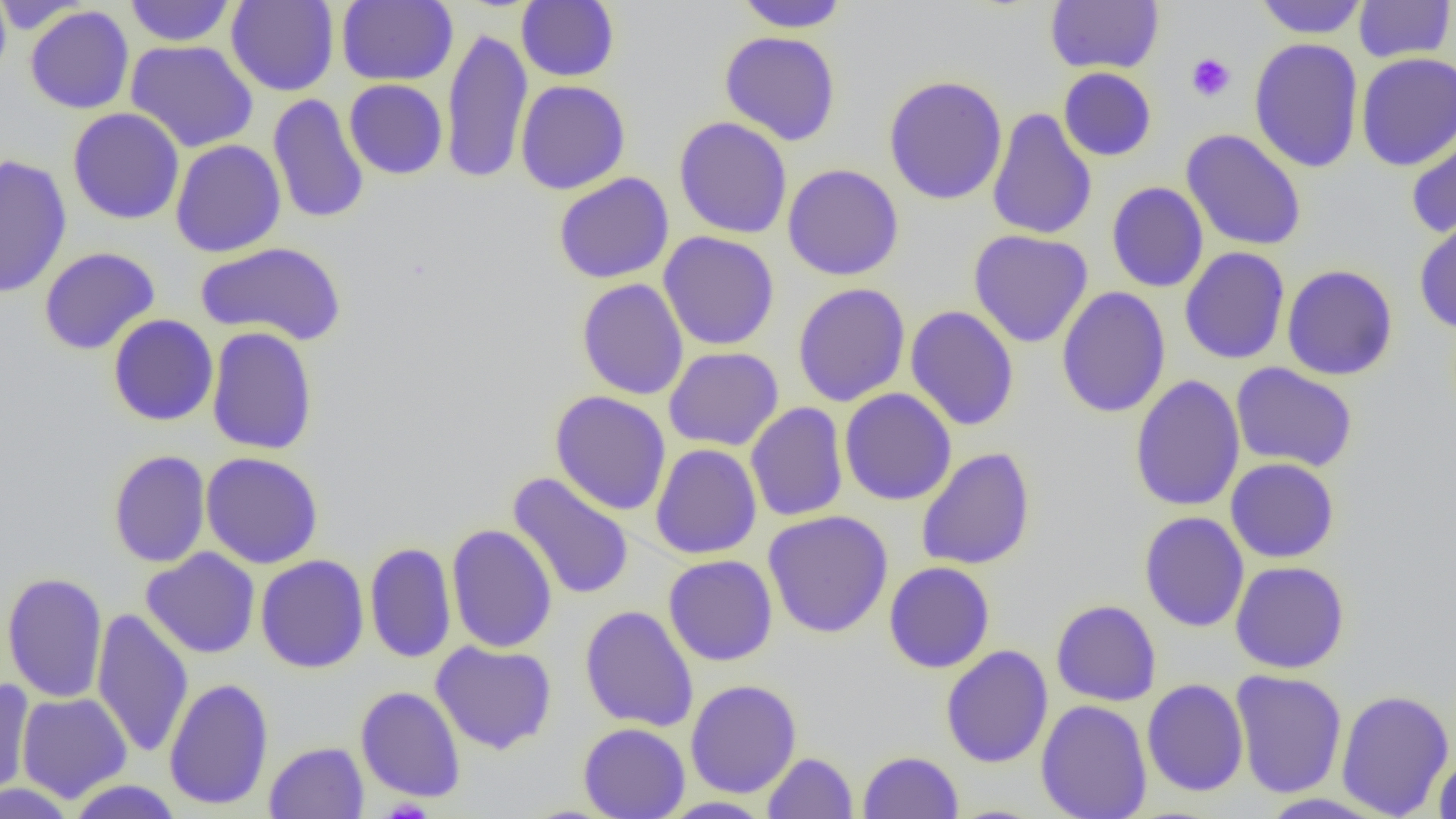 Approximate bounding boxes as named x1/y1/x2/y2 corners in pixels. Platelet locations: (x1=1186, y1=53, x2=1236, y2=102). Uninfected red blood cell locations: (x1=0, y1=0, x2=11, y2=86), (x1=124, y1=0, x2=236, y2=47), (x1=226, y1=0, x2=339, y2=96), (x1=336, y1=0, x2=458, y2=86), (x1=733, y1=0, x2=850, y2=33), (x1=1254, y1=0, x2=1368, y2=38), (x1=1353, y1=0, x2=1455, y2=63), (x1=0, y1=1, x2=91, y2=36), (x1=516, y1=1, x2=620, y2=82), (x1=1046, y1=1, x2=1164, y2=74), (x1=25, y1=6, x2=134, y2=113), (x1=440, y1=28, x2=533, y2=185), (x1=719, y1=30, x2=841, y2=146), (x1=1249, y1=37, x2=1364, y2=173), (x1=126, y1=39, x2=258, y2=153), (x1=1356, y1=52, x2=1456, y2=171), (x1=1058, y1=67, x2=1157, y2=162), (x1=883, y1=75, x2=1008, y2=205), (x1=344, y1=79, x2=448, y2=179), (x1=515, y1=80, x2=631, y2=195), (x1=268, y1=93, x2=369, y2=224), (x1=68, y1=107, x2=185, y2=224), (x1=987, y1=107, x2=1097, y2=241), (x1=674, y1=116, x2=792, y2=239), (x1=1405, y1=118, x2=1456, y2=241), (x1=1181, y1=129, x2=1307, y2=251), (x1=170, y1=139, x2=286, y2=257), (x1=0, y1=154, x2=72, y2=298), (x1=783, y1=163, x2=904, y2=281), (x1=553, y1=172, x2=674, y2=284), (x1=1106, y1=182, x2=1209, y2=292), (x1=1414, y1=216, x2=1456, y2=334), (x1=968, y1=229, x2=1094, y2=348), (x1=659, y1=231, x2=780, y2=350), (x1=195, y1=241, x2=347, y2=346), (x1=39, y1=247, x2=160, y2=355), (x1=1179, y1=247, x2=1290, y2=365), (x1=1281, y1=264, x2=1399, y2=381), (x1=576, y1=278, x2=689, y2=400), (x1=793, y1=283, x2=910, y2=407), (x1=1056, y1=286, x2=1171, y2=418), (x1=905, y1=305, x2=1019, y2=431), (x1=107, y1=314, x2=218, y2=426), (x1=206, y1=326, x2=319, y2=455), (x1=663, y1=346, x2=784, y2=451), (x1=1230, y1=362, x2=1358, y2=472), (x1=1129, y1=375, x2=1245, y2=512), (x1=839, y1=388, x2=957, y2=505), (x1=549, y1=391, x2=671, y2=515), (x1=746, y1=402, x2=849, y2=522), (x1=650, y1=443, x2=762, y2=559), (x1=916, y1=447, x2=1036, y2=570), (x1=108, y1=449, x2=210, y2=568), (x1=201, y1=451, x2=324, y2=569), (x1=1225, y1=458, x2=1339, y2=563), (x1=508, y1=473, x2=634, y2=601), (x1=763, y1=510, x2=893, y2=638), (x1=1138, y1=512, x2=1249, y2=632), (x1=445, y1=523, x2=558, y2=653), (x1=364, y1=541, x2=457, y2=664), (x1=141, y1=547, x2=260, y2=659), (x1=255, y1=554, x2=370, y2=673), (x1=663, y1=554, x2=778, y2=666), (x1=1230, y1=560, x2=1350, y2=674), (x1=884, y1=561, x2=996, y2=673), (x1=1, y1=572, x2=108, y2=703), (x1=1051, y1=599, x2=1161, y2=706), (x1=579, y1=605, x2=699, y2=732), (x1=92, y1=607, x2=193, y2=759), (x1=430, y1=640, x2=557, y2=754), (x1=940, y1=645, x2=1053, y2=768), (x1=1230, y1=669, x2=1348, y2=799), (x1=163, y1=678, x2=274, y2=810), (x1=1141, y1=678, x2=1249, y2=796), (x1=0, y1=679, x2=35, y2=802), (x1=685, y1=679, x2=802, y2=798), (x1=355, y1=686, x2=467, y2=803), (x1=1335, y1=688, x2=1454, y2=818), (x1=16, y1=692, x2=132, y2=802), (x1=1036, y1=699, x2=1153, y2=819), (x1=578, y1=723, x2=690, y2=819), (x1=264, y1=741, x2=369, y2=818), (x1=1434, y1=749, x2=1456, y2=818), (x1=858, y1=750, x2=964, y2=818), (x1=763, y1=752, x2=858, y2=818), (x1=66, y1=780, x2=185, y2=818), (x1=0, y1=782, x2=76, y2=819), (x1=1255, y1=793, x2=1394, y2=818), (x1=657, y1=796, x2=774, y2=818). Slide-level diagnosis: no evidence of blood parasites. Light microscopy. Image is 1456×819 pixels. Thin blood film. Single field of view. 1000x magnification.